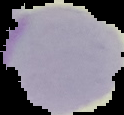 The area outside the segmented cell region is set to black. Image is 124×115 pixels. From a thin blood smear. Result: negative for Plasmodium parasites.